Assess this cell for malaria.
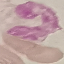

Uninfected.

image type = cell patch, automatically extracted from a larger field of view and resized to 64 × 64 pixels
capture = smartphone camera at the microscope eyepiece
stain = Giemsa
preparation = thin blood smear